Assess the morphology of the erythrocytes.
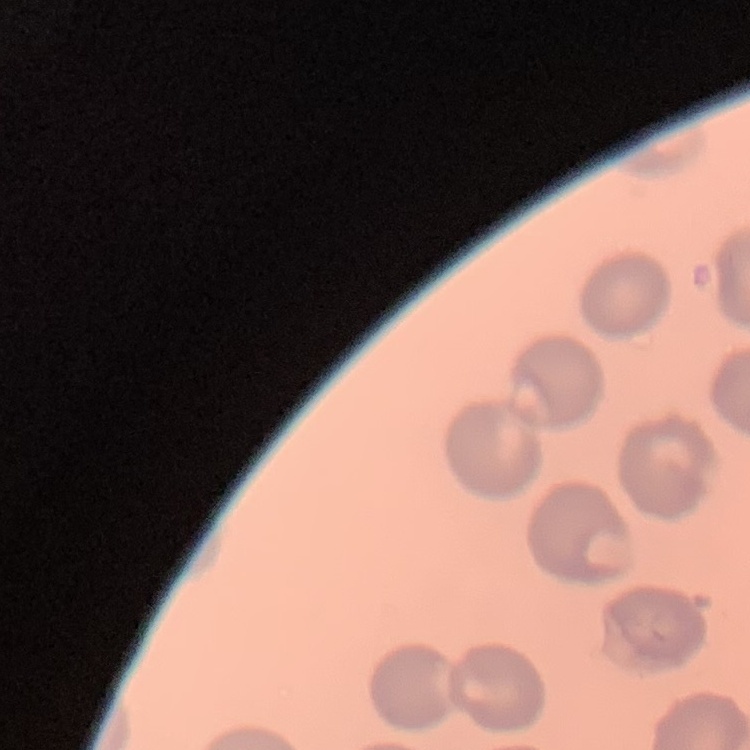

They show no rouleaux formation.

{
  "stain": "Field's or Giemsa",
  "image_type": "one tile cut from a larger photomicrograph",
  "preparation": "thin blood film"
}